Assess for Plasmodium parasites.
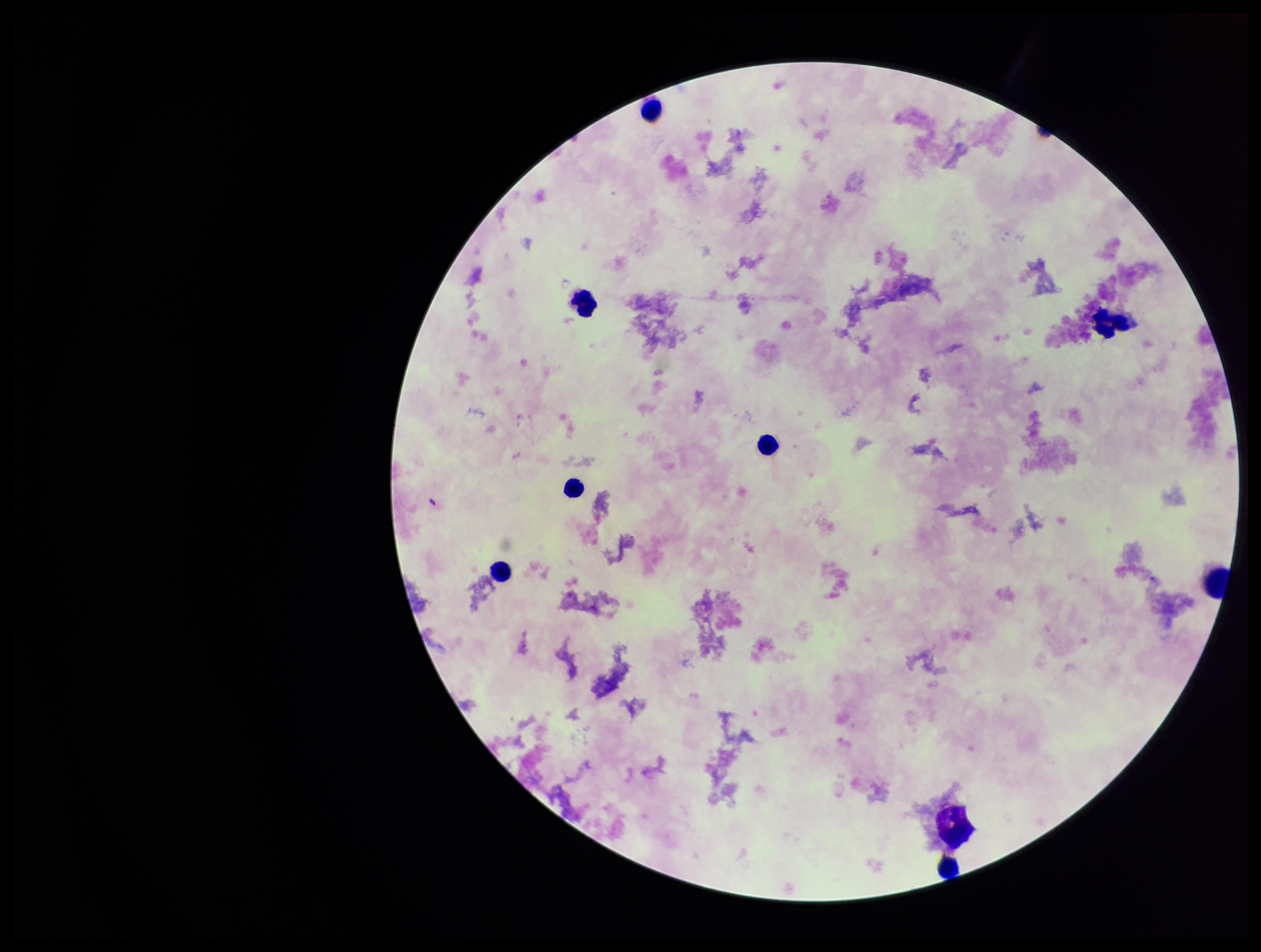

None seen.

Giemsa stain. Leukocyte count: 8. Image is 1261×952 pixels. Photographed through the microscope eyepiece with a smartphone camera. Preparation: thick smear. Single field of view. Parasite count: 0. Patient malaria status: negative.